Locate every blood parasite and identify its species.
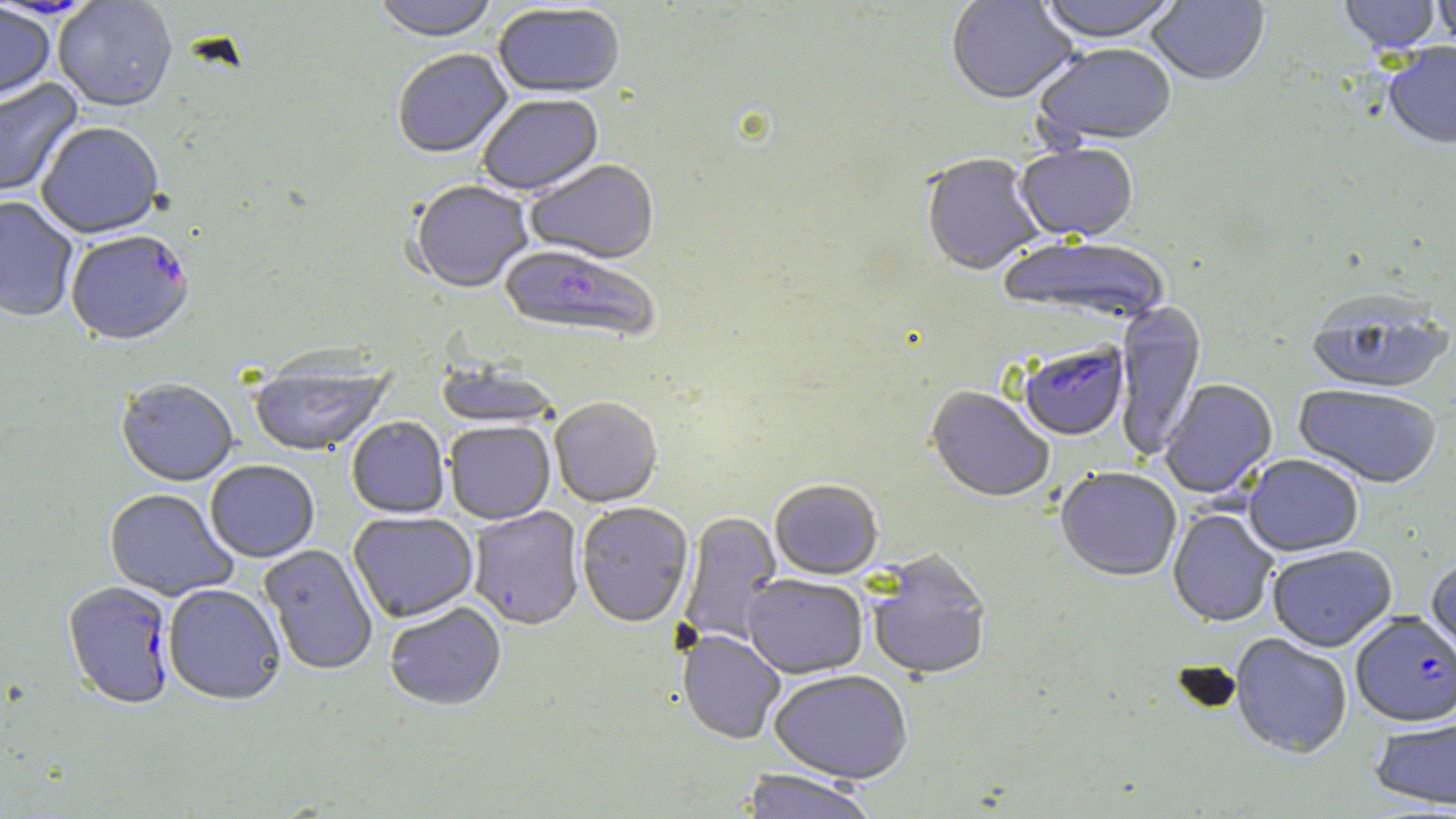
Approximate bounding boxes as [x1, y1, x2, y2] in pixels.
Plasmodium falciparum-infected red blood cells: [66, 233, 195, 348], [499, 246, 660, 345], [1018, 343, 1130, 442], [62, 582, 175, 711], [1351, 613, 1456, 727].
No Plasmodium ovale, Plasmodium malariae, Plasmodium vivax, Babesia divergens, or Trypanosoma brucei observed.

Uninfected red blood cell locations: [371, 0, 500, 45], [946, 0, 1079, 107], [1036, 0, 1183, 46], [1146, 0, 1270, 88], [1338, 0, 1441, 56], [1431, 0, 1456, 51], [0, 1, 101, 21], [52, 1, 177, 114], [0, 3, 55, 105], [493, 5, 626, 101], [1033, 45, 1177, 150], [1384, 45, 1456, 152], [393, 51, 513, 161], [0, 79, 84, 199], [478, 96, 604, 197], [36, 125, 164, 241], [1015, 145, 1139, 244], [921, 155, 1046, 278], [525, 161, 660, 266], [409, 182, 533, 295], [0, 198, 78, 323], [997, 237, 1171, 327], [1305, 295, 1454, 397], [1113, 301, 1206, 459], [248, 357, 393, 458], [434, 359, 562, 430], [1160, 380, 1278, 499], [116, 381, 238, 488], [1293, 385, 1442, 489], [926, 387, 1054, 504], [551, 398, 663, 508], [347, 417, 449, 519], [445, 422, 555, 525], [1244, 455, 1364, 558], [206, 461, 320, 564], [1055, 468, 1181, 583], [770, 480, 883, 580], [104, 489, 237, 601], [576, 503, 693, 629], [468, 508, 584, 631], [1167, 509, 1278, 628], [678, 511, 783, 646], [348, 512, 479, 624], [259, 544, 378, 676], [1268, 545, 1397, 652], [866, 550, 993, 682], [1425, 557, 1456, 680], [743, 575, 868, 679], [163, 585, 286, 707], [384, 603, 506, 713], [677, 631, 786, 745], [1229, 634, 1352, 759], [769, 670, 913, 784], [1369, 716, 1456, 811], [738, 770, 880, 819]. Slide-level diagnosis: Plasmodium falciparum. May-Grünwald-Giemsa stain. Image is 1456×819 pixels. Thin blood film. One field of a larger specimen. 1000x magnification. Optical microscopy.